Classify this cell by malaria status.
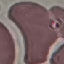

Uninfected.

{
  "stain": "Giemsa",
  "capture": "smartphone camera at the microscope eyepiece",
  "preparation": "thin blood film",
  "image_type": "cell patch, automatically extracted from a larger field of view and resized to 64 × 64 pixels"
}